Locate every Plasmodium parasite.
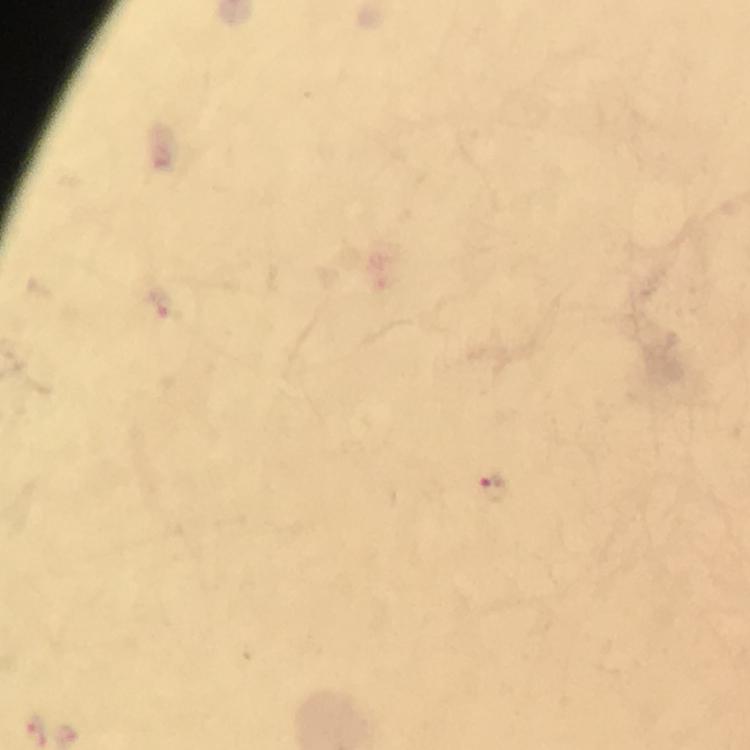
Approximate centers as [x, y] in pixels.
Plasmodium parasites: [494, 489].

Immersion oil was used. Giemsa-stained preparation. Thick blood smear. Image is 750×750 pixels. Smartphone photograph taken through a microscope. From a malaria diagnostic workup. A crop from one field of view. At 100x magnification.